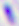

identification = Toxoplasma gondii
modality = micrograph
magnification = 400x